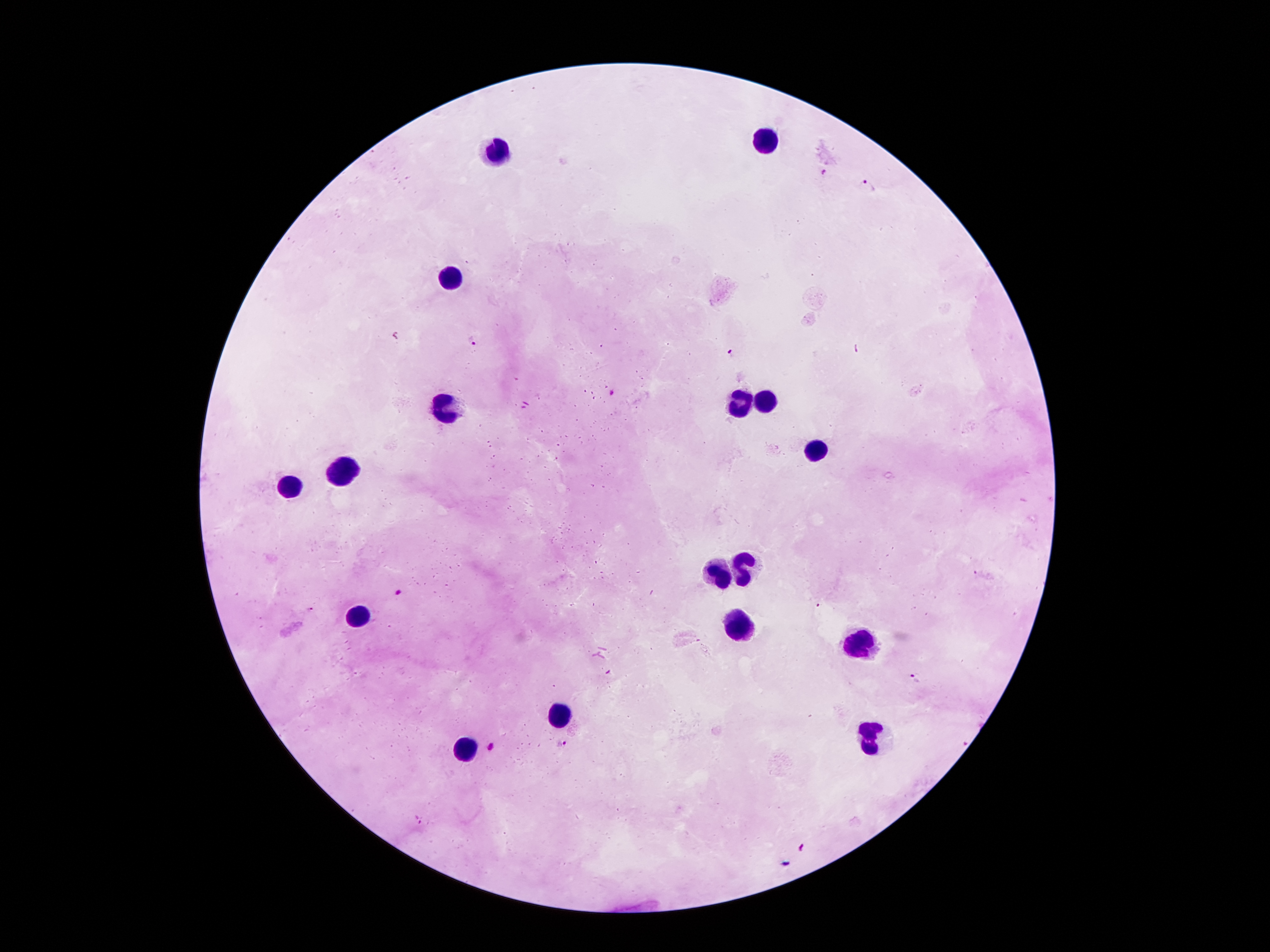

Approximate object centers, in pixels from the top-left corner. Leukocyte locations: (x=766, y=139), (x=499, y=149), (x=450, y=275), (x=766, y=399), (x=737, y=404), (x=445, y=406), (x=816, y=453), (x=341, y=475), (x=292, y=488), (x=747, y=562), (x=722, y=572), (x=358, y=614), (x=742, y=623), (x=855, y=643), (x=561, y=717), (x=870, y=740), (x=465, y=747). Plasmodium parasite locations: (x=823, y=173), (x=868, y=184), (x=471, y=341), (x=733, y=353), (x=614, y=392), (x=400, y=591), (x=913, y=680), (x=563, y=744), (x=491, y=746), (x=418, y=820), (x=802, y=846). Thick blood film. One field from this slide. 100x magnification. Patient malaria status: infected with Plasmodium falciparum. Image is 1270×952 pixels. Giemsa-stained preparation. Smartphone photograph taken through the microscope eyepiece.